Classify this cell by malaria status.
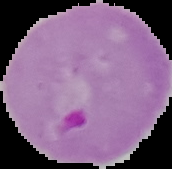

It is parasitized.

From a thin blood film. The area outside the segmented cell region is set to black. Image is 172×169 pixels.